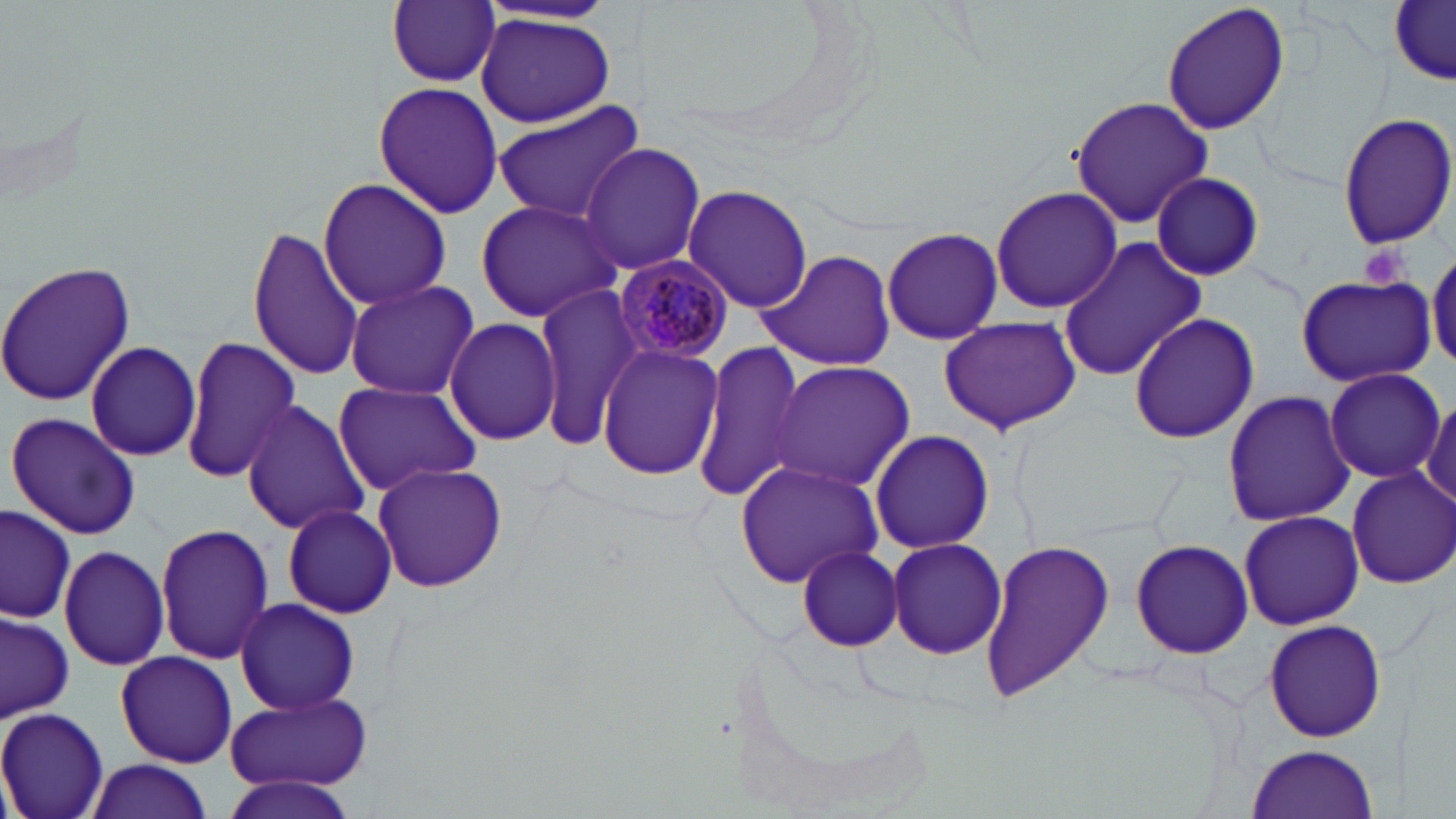

Summary:
  - Coordinate format: approximate bounding boxes as [x1, y1, x2, y2] in pixels
  - Platelet locations: [1356, 244, 1411, 292]
  - Plasmodium malariae-infected red blood cell locations: [614, 254, 735, 364]
  - Uninfected red blood cell locations: [387, 0, 499, 87], [1160, 0, 1291, 138], [1390, 3, 1454, 85], [475, 13, 617, 127], [373, 82, 504, 218], [1069, 95, 1212, 230], [492, 101, 647, 224], [1334, 111, 1454, 251], [579, 141, 706, 276], [1150, 172, 1265, 280], [317, 176, 451, 311], [682, 185, 811, 314], [991, 187, 1123, 314], [474, 198, 624, 323], [245, 224, 364, 382], [881, 226, 1003, 346], [1059, 237, 1209, 381], [1427, 248, 1456, 372], [759, 249, 897, 369], [0, 261, 137, 405], [1297, 275, 1435, 387], [343, 278, 480, 399], [533, 283, 644, 444], [1127, 311, 1259, 446], [444, 315, 562, 447], [938, 315, 1081, 436], [180, 335, 299, 484], [84, 341, 202, 462], [691, 342, 807, 504], [597, 343, 725, 480], [767, 360, 916, 492], [33, 364, 175, 517], [1323, 366, 1446, 484], [331, 378, 481, 496], [1222, 388, 1355, 527], [1421, 395, 1456, 510], [239, 398, 371, 538], [6, 412, 142, 540], [871, 428, 995, 554], [735, 460, 885, 592], [371, 461, 509, 594], [1346, 466, 1456, 590], [280, 503, 399, 619], [1, 505, 77, 624], [1236, 509, 1364, 630], [152, 523, 273, 666], [885, 537, 1007, 660], [978, 538, 1117, 702], [1131, 539, 1255, 659], [58, 543, 172, 671], [795, 544, 905, 651], [234, 596, 361, 716], [0, 611, 73, 721], [1261, 617, 1388, 743], [116, 649, 237, 768], [222, 693, 373, 794], [0, 706, 110, 819], [1246, 745, 1381, 818], [85, 758, 214, 819], [221, 774, 365, 819]
  - Slide-level diagnosis: Plasmodium malariae
  - Magnification: 1000x
  - Field of view: single
  - Image size: 1456×819 pixels
  - Modality: light microscopy
  - Stain: May-Grünwald-Giemsa
  - Preparation: thin blood film